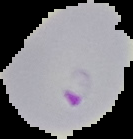
image_size: 133×139 pixels
preparation: thin blood film
image_type: segmented cell region on a black background
result: malaria parasites detected